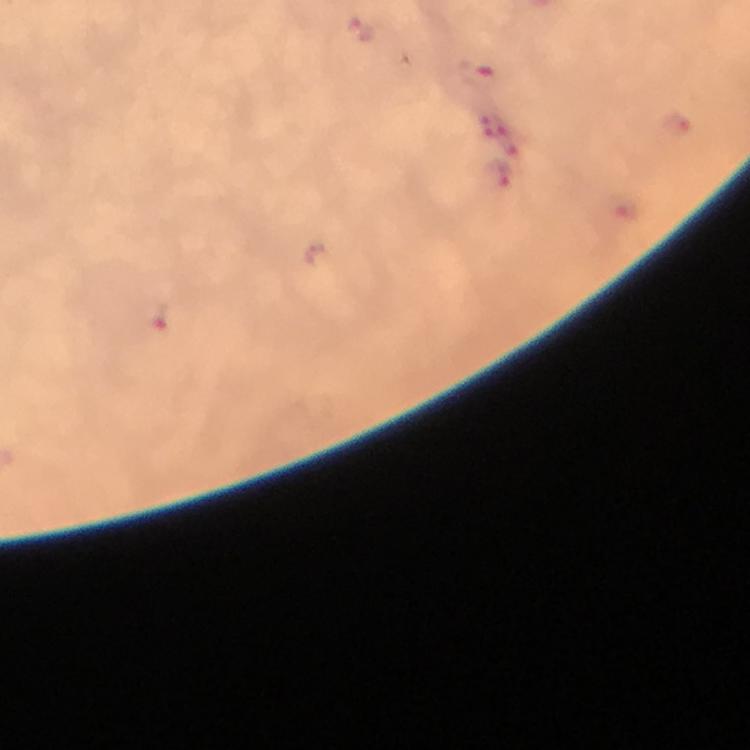
Approximate object centers, in pixels from the top-left corner.
Summary:
  - Plasmodium parasite locations: (x=359, y=30), (x=476, y=71), (x=676, y=126), (x=503, y=129), (x=502, y=172), (x=162, y=314)
  - Stain: Giemsa
  - Capture: smartphone camera through the microscope
  - Immersion oil: used
  - Cropped from: a single field of view
  - Context: from a diagnostic examination for malaria
  - Magnification: 100x
  - Preparation: thick blood film
  - Image size: 750×750 pixels